Report the malaria status of this cell.
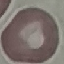

It is uninfected.

image_type: cell patch, automatically extracted from a larger field of view and resized to 64 × 64 pixels
capture: smartphone through the microscope eyepiece
preparation: thin blood film
stain: Giemsa